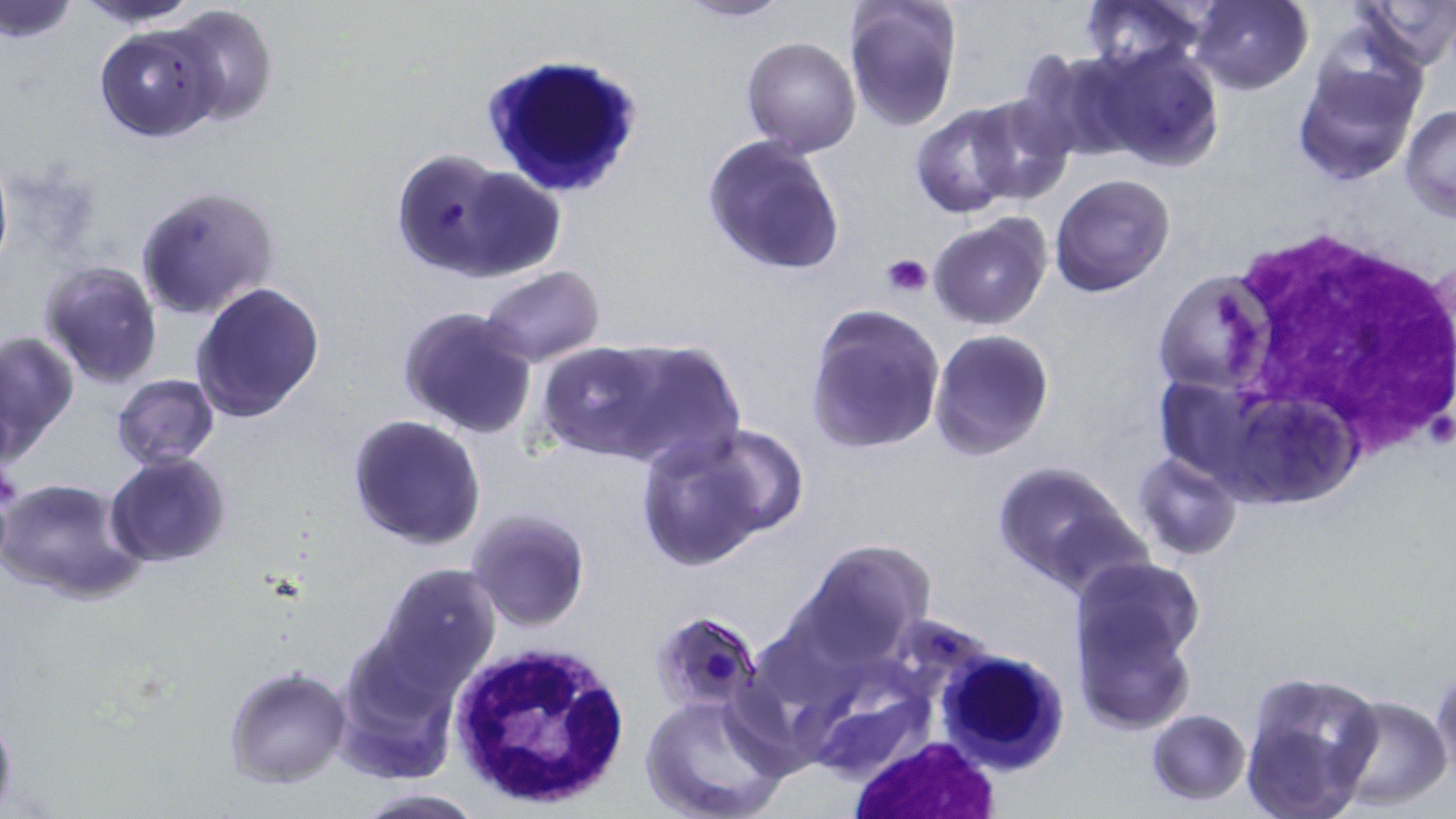

Approximate bounding boxes as named x1/y1/x2/y2 corners in pixels. White blood cell locations: (x1=480, y1=53, x2=647, y2=196), (x1=1213, y1=221, x2=1456, y2=468), (x1=449, y1=641, x2=628, y2=806), (x1=936, y1=648, x2=1068, y2=773), (x1=850, y1=738, x2=1000, y2=819). Plasmodium falciparum-infected red blood cell locations: (x1=390, y1=148, x2=503, y2=281), (x1=902, y1=616, x2=988, y2=671). Uninfected red blood cell locations: (x1=0, y1=0, x2=80, y2=44), (x1=77, y1=0, x2=202, y2=28), (x1=676, y1=0, x2=794, y2=23), (x1=1081, y1=0, x2=1211, y2=78), (x1=1187, y1=0, x2=1312, y2=95), (x1=1350, y1=0, x2=1454, y2=71), (x1=842, y1=1, x2=963, y2=132), (x1=165, y1=4, x2=278, y2=128), (x1=93, y1=22, x2=220, y2=142), (x1=741, y1=36, x2=862, y2=157), (x1=1086, y1=39, x2=1226, y2=171), (x1=1018, y1=50, x2=1138, y2=159), (x1=1291, y1=57, x2=1422, y2=186), (x1=964, y1=97, x2=1077, y2=207), (x1=909, y1=104, x2=1025, y2=217), (x1=1399, y1=105, x2=1456, y2=220), (x1=702, y1=133, x2=846, y2=276), (x1=463, y1=168, x2=564, y2=280), (x1=1050, y1=172, x2=1177, y2=298), (x1=134, y1=185, x2=279, y2=321), (x1=928, y1=213, x2=1054, y2=331), (x1=39, y1=260, x2=163, y2=389), (x1=479, y1=265, x2=606, y2=367), (x1=1154, y1=271, x2=1270, y2=395), (x1=190, y1=281, x2=325, y2=422), (x1=396, y1=305, x2=537, y2=440), (x1=804, y1=306, x2=945, y2=455), (x1=0, y1=329, x2=78, y2=458), (x1=929, y1=329, x2=1055, y2=461), (x1=588, y1=339, x2=747, y2=472), (x1=536, y1=341, x2=675, y2=458), (x1=112, y1=375, x2=219, y2=469), (x1=1156, y1=379, x2=1271, y2=505), (x1=1240, y1=392, x2=1366, y2=510), (x1=346, y1=414, x2=486, y2=550), (x1=635, y1=430, x2=782, y2=572), (x1=1134, y1=452, x2=1241, y2=561), (x1=105, y1=454, x2=230, y2=568), (x1=990, y1=459, x2=1141, y2=594), (x1=1, y1=476, x2=144, y2=605), (x1=466, y1=509, x2=591, y2=633), (x1=798, y1=541, x2=934, y2=663), (x1=1069, y1=556, x2=1204, y2=677), (x1=376, y1=563, x2=500, y2=684), (x1=1071, y1=597, x2=1196, y2=735), (x1=335, y1=654, x2=455, y2=781), (x1=1432, y1=664, x2=1455, y2=783), (x1=223, y1=666, x2=351, y2=789), (x1=1240, y1=673, x2=1381, y2=819), (x1=809, y1=679, x2=929, y2=784), (x1=639, y1=690, x2=793, y2=819), (x1=1332, y1=694, x2=1452, y2=809), (x1=1147, y1=709, x2=1250, y2=804), (x1=354, y1=787, x2=487, y2=818). Platelet locations: (x1=881, y1=251, x2=934, y2=298). Slide-level diagnosis: Plasmodium falciparum. Image is 1456×819 pixels. May-Grünwald-Giemsa-stained preparation. Thin blood smear. Light microscopy. Single field of view. 1000x magnification.